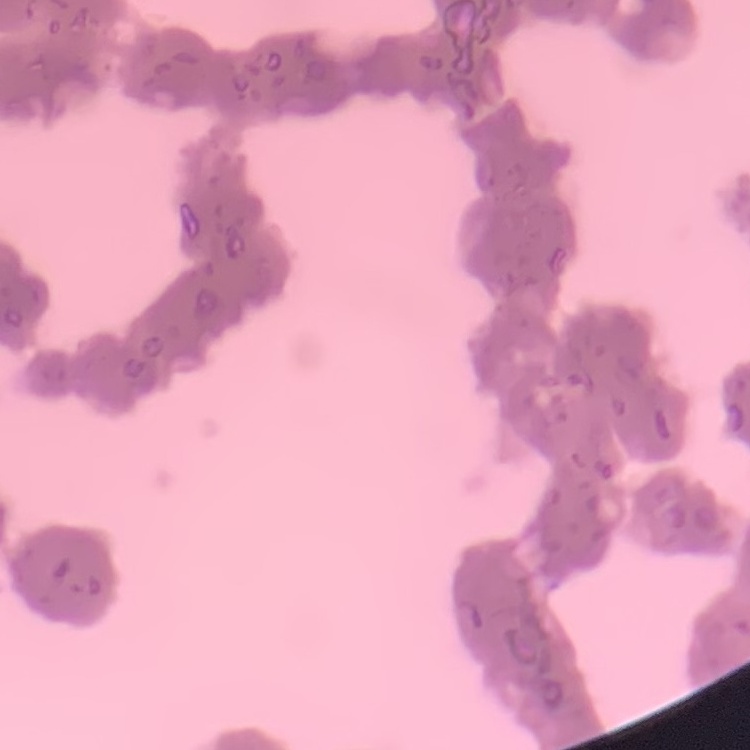

{
  "erythrocyte_morphology": "rouleaux formation",
  "image_type": "one tile cut from a larger photomicrograph",
  "stain": "Field's or Giemsa",
  "preparation": "thin peripheral smear"
}